Locate every Plasmodium parasite.
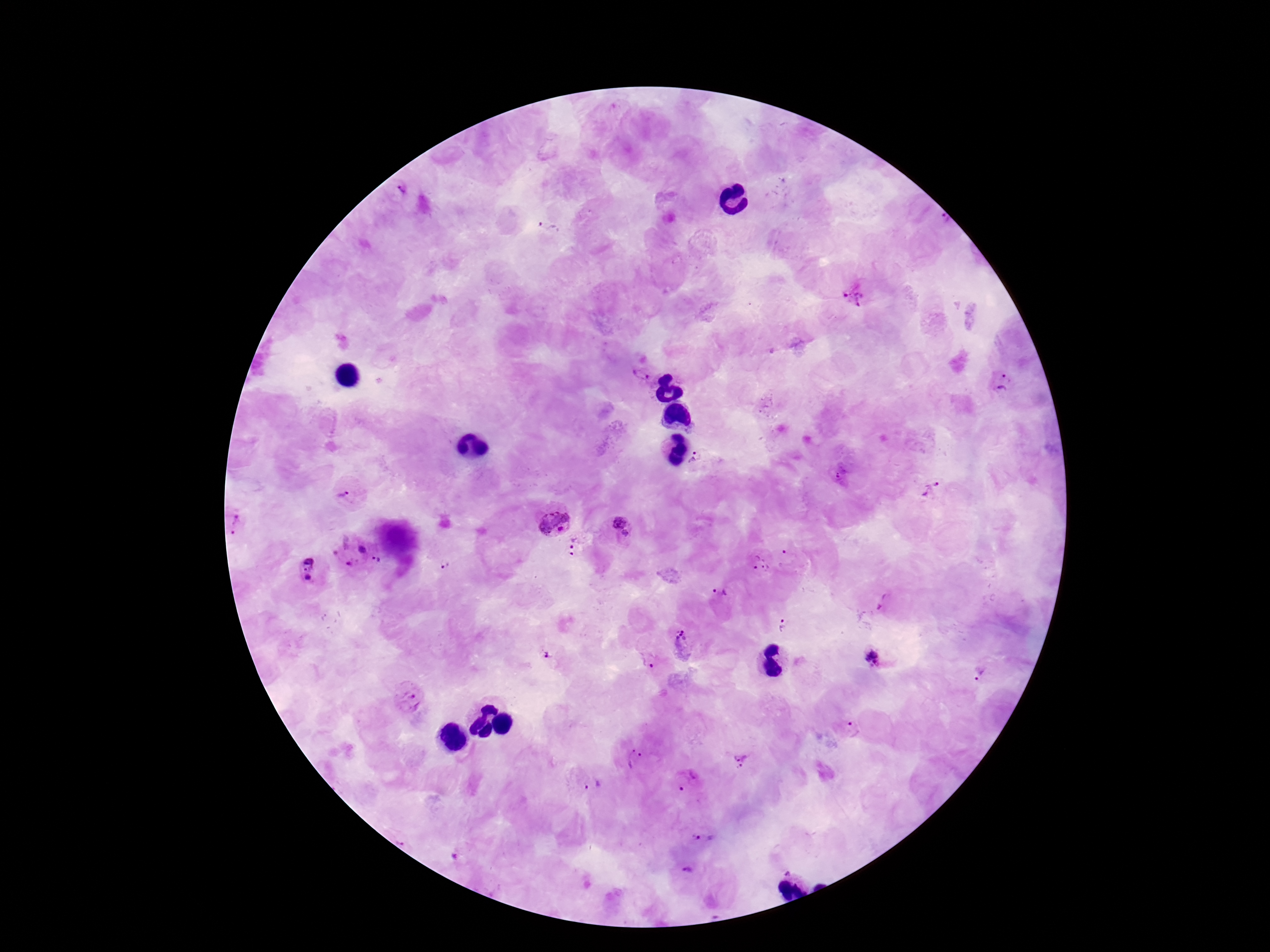
Approximate centers as (x, y) in pixels.
Plasmodium parasites: (398, 188), (548, 225), (859, 291), (643, 372), (1002, 383), (697, 458), (845, 473), (932, 488), (350, 493), (554, 519), (237, 520), (621, 528), (575, 544), (351, 549), (789, 557), (382, 562), (447, 563), (756, 564), (306, 570), (722, 603), (786, 627), (680, 644), (546, 654), (872, 656), (649, 660), (979, 675), (410, 697), (850, 730), (633, 758), (741, 759), (687, 782), (591, 785), (702, 835), (689, 869).

100x magnification. Photographed through the microscope eyepiece with a smartphone camera. Giemsa stain. Image is 1270×952 pixels. One field from this slide. Thick peripheral-blood smear. Patient malaria status: infected.